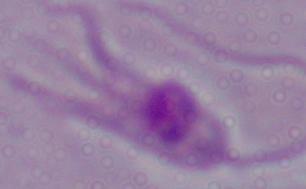

Captured at 1000x magnification. Photomicrograph. A Leishmania parasite is shown.